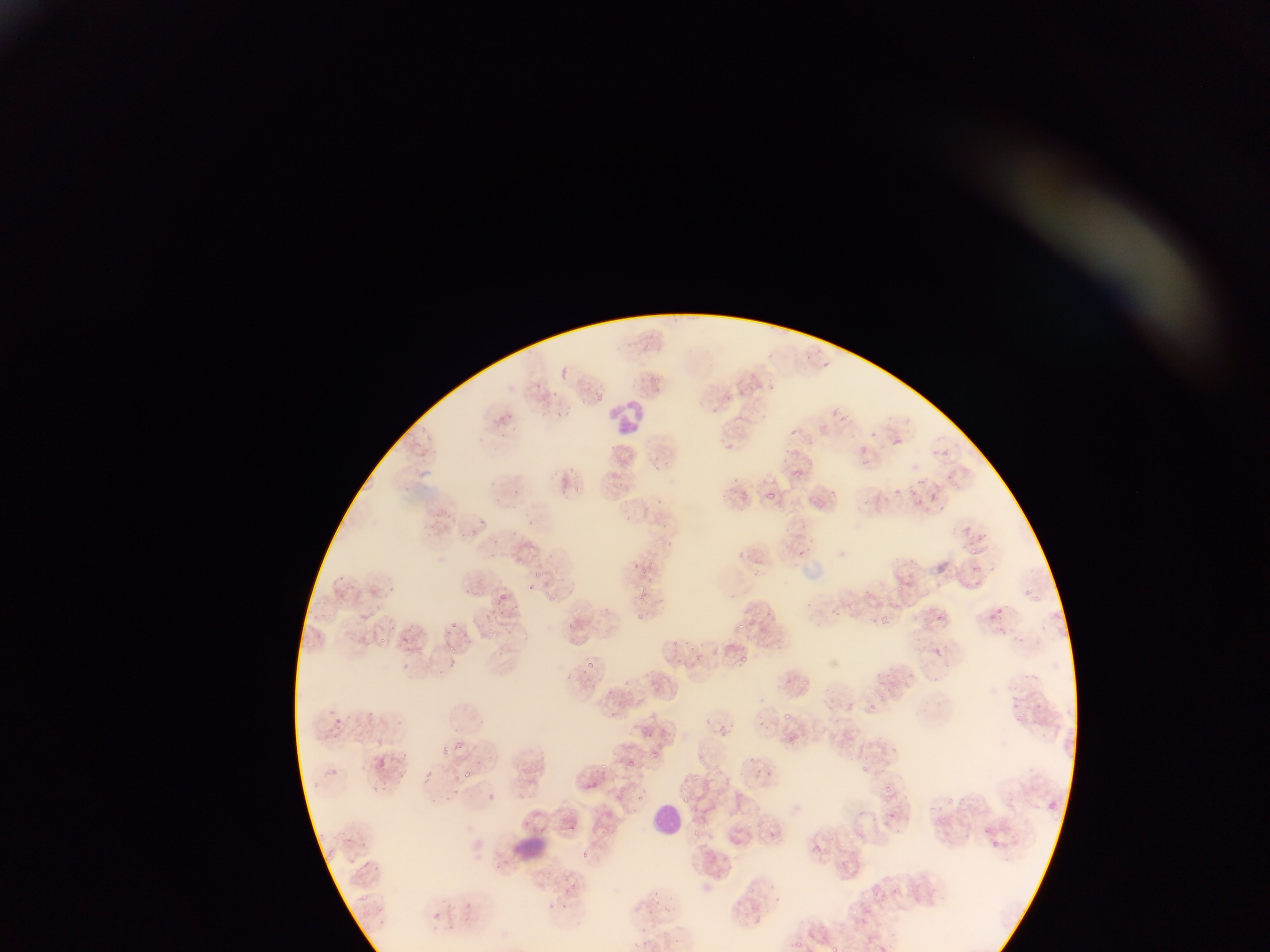
Approximate bounding boxes as left top right bottom in pixels.
Summary:
  - Leukocyte locations: 611 393 654 439; 641 796 693 849
  - Plasmodium parasite locations (subset; some below the resolvable size): 823 359 831 368; 594 394 605 405; 830 407 840 415; 552 408 564 418; 838 410 853 424; 789 424 802 437; 868 427 876 439; 498 431 509 443; 427 434 433 442; 890 436 900 446; 859 441 867 456; 607 445 618 452; 789 446 798 456; 934 446 942 454; 941 446 955 460; 653 454 663 464; 805 455 815 466; 652 463 660 476; 567 465 581 475; 790 466 803 481; 945 471 953 481; 916 477 933 488; 483 479 497 490; 617 480 626 492; 404 485 414 495; 894 486 907 497; 513 488 523 499; 561 489 568 497; 764 489 773 499; 830 490 839 496; 930 491 941 501; 916 497 921 505; 655 498 663 508; 623 513 633 522; 475 516 486 527; 525 519 535 527; 963 522 971 532; 425 526 436 537; 510 528 520 539; 973 529 993 543; 465 531 478 540; 795 531 803 538; 736 547 746 563; 969 548 977 553; 799 550 807 563; 488 553 498 561; 635 565 657 579; 970 566 982 575; 535 569 541 577; 337 574 345 578; 348 580 360 593; 528 582 536 591; 386 583 397 594; 463 585 471 594; 894 585 905 595; 500 589 513 602; 338 591 348 598; 729 591 741 601; 513 602 523 610; 827 606 838 619; 996 606 1005 613; 490 608 502 618; 937 610 948 623; 637 611 650 627; 876 614 897 630; 450 617 467 625; 386 622 398 636; 735 623 747 633; 759 626 769 635; 485 630 493 637; 670 637 683 647; 443 641 455 649; 760 641 768 649; 413 644 421 653; 738 655 746 664; 446 656 458 669; 674 656 684 667; 587 659 603 669; 399 662 413 670; 801 679 809 684; 870 703 877 714; 328 708 338 716; 362 709 375 719; 783 712 789 723; 702 716 713 727; 336 718 344 726; 640 722 644 733; 717 724 731 735; 377 735 385 743; 456 738 466 748; 787 738 795 744; 443 747 453 759; 648 752 658 759; 750 755 758 766; 377 756 387 772; 626 756 639 767; 700 756 707 767; 862 763 869 771; 602 764 605 772; 462 766 474 783; 326 769 347 782; 427 769 442 780; 399 773 406 783; 683 774 695 784; 589 781 597 786; 883 783 894 795; 452 789 464 795; 486 793 494 801; 887 794 893 803; 1048 799 1057 809; 1033 801 1039 811; 565 805 575 814; 694 828 706 839; 858 832 868 844; 580 854 589 859; 370 862 378 867; 748 886 753 894; 360 892 371 903; 654 896 666 908; 461 900 474 910; 432 911 443 919; 793 934 803 950; 833 944 843 952 | approximate x y pixel centers of objects too small to bound: 979 582; 383 642; 628 683; 938 817; 947 832
  - Image size: 1270×952 pixels
  - Country: Ghana
  - Field of view: single
  - Capture: mobile-phone photograph through a microscope
  - Preparation: thin blood smear